Identify the parasite.
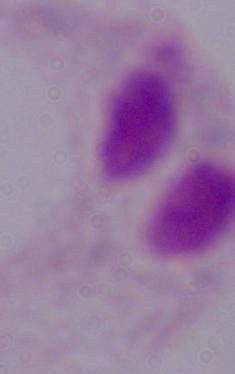
A trichomonad.

Summary:
  - Modality: photomicrograph
  - Magnification: 1000x